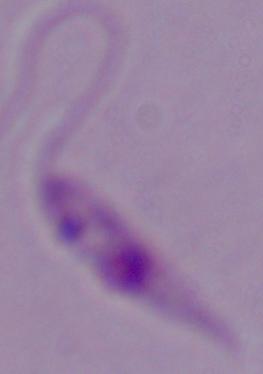

Summary:
  - Modality: photomicrograph
  - Identification: Leishmania
  - Magnification: 1000x